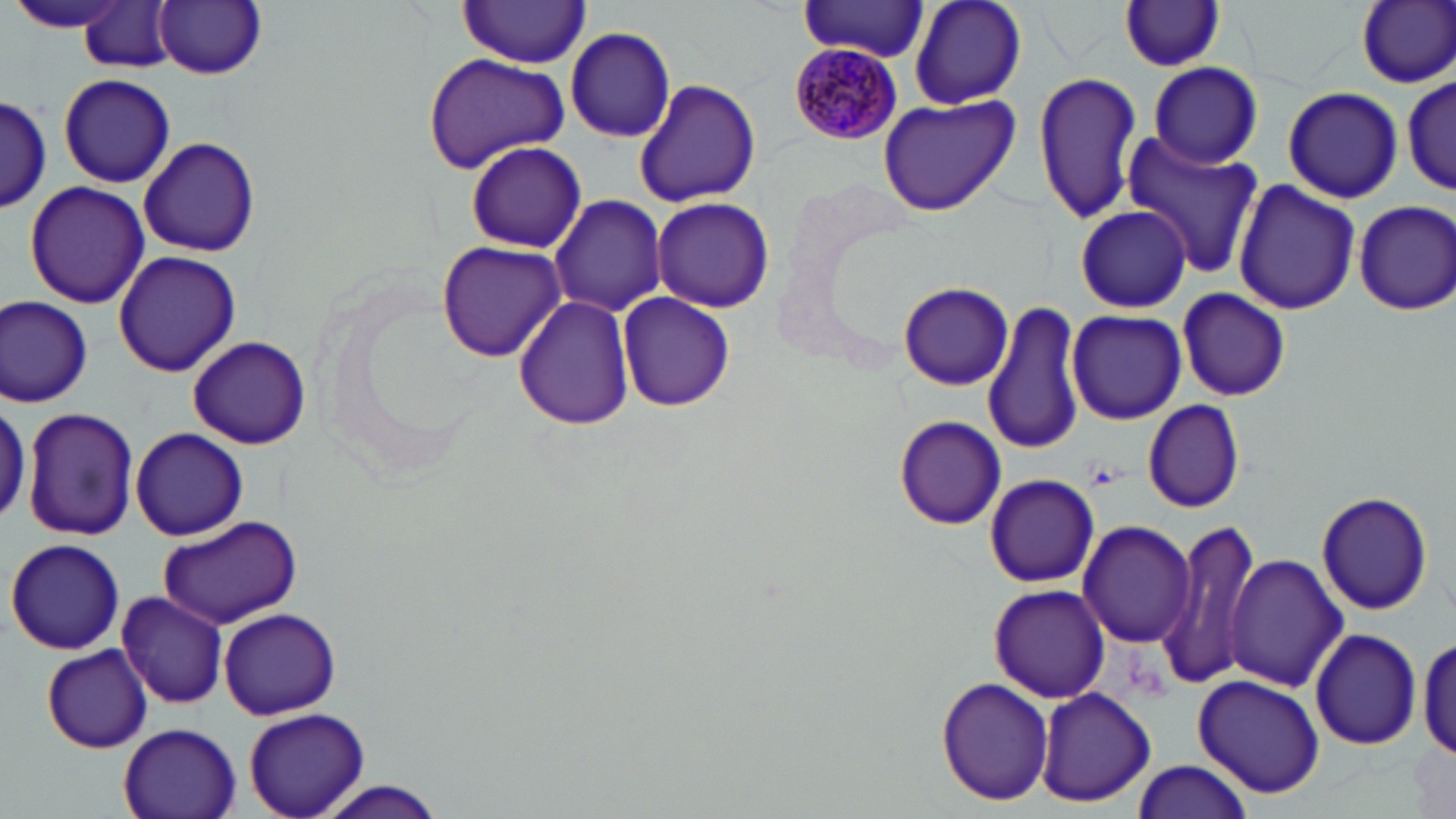
Approximate bounding boxes as (x1, y1, x2, y2) in pixels. Plasmodium malariae-infected red blood cell locations: (789, 33, 905, 145). Uninfected red blood cell locations: (909, 0, 1027, 111), (1355, 0, 1456, 88), (6, 1, 135, 34), (155, 1, 266, 79), (1117, 1, 1228, 73), (78, 2, 179, 73), (455, 2, 593, 67), (797, 2, 929, 61), (566, 26, 679, 142), (421, 53, 573, 172), (1149, 61, 1263, 169), (1031, 69, 1142, 225), (1401, 71, 1452, 199), (58, 72, 176, 188), (633, 79, 762, 209), (1283, 86, 1404, 203), (0, 96, 51, 212), (877, 96, 1020, 215), (1121, 135, 1261, 279), (140, 138, 260, 256), (462, 139, 588, 253), (1233, 178, 1360, 317), (24, 180, 150, 309), (550, 194, 666, 318), (652, 196, 775, 313), (1352, 199, 1456, 314), (1075, 203, 1192, 312), (435, 241, 568, 362), (113, 249, 240, 377), (897, 281, 1014, 390), (1176, 287, 1290, 403), (616, 292, 736, 413), (0, 295, 92, 408), (512, 295, 635, 430), (985, 300, 1087, 458), (1067, 308, 1186, 424), (187, 334, 311, 451), (0, 397, 30, 523), (1142, 399, 1245, 514), (22, 407, 139, 541), (894, 415, 1008, 530), (131, 428, 249, 540), (985, 474, 1099, 587), (1316, 491, 1433, 615), (155, 514, 300, 628), (1164, 518, 1261, 687), (1079, 520, 1196, 647), (5, 538, 125, 655), (1227, 553, 1349, 692), (989, 582, 1108, 704), (117, 590, 226, 709), (218, 608, 341, 720), (1310, 628, 1424, 751), (1416, 630, 1455, 765), (42, 645, 152, 754), (1194, 675, 1324, 797), (937, 679, 1054, 807), (1035, 688, 1157, 807), (243, 706, 371, 815), (118, 724, 242, 819), (1129, 760, 1255, 819), (308, 778, 453, 819). Platelet locations: (1088, 461, 1121, 488). Slide-level diagnosis: Plasmodium malariae. Image is 1456×819 pixels. Single field of view. Thin blood film. May-Grünwald-Giemsa-stained preparation. 1000x magnification. Optical microscopy.